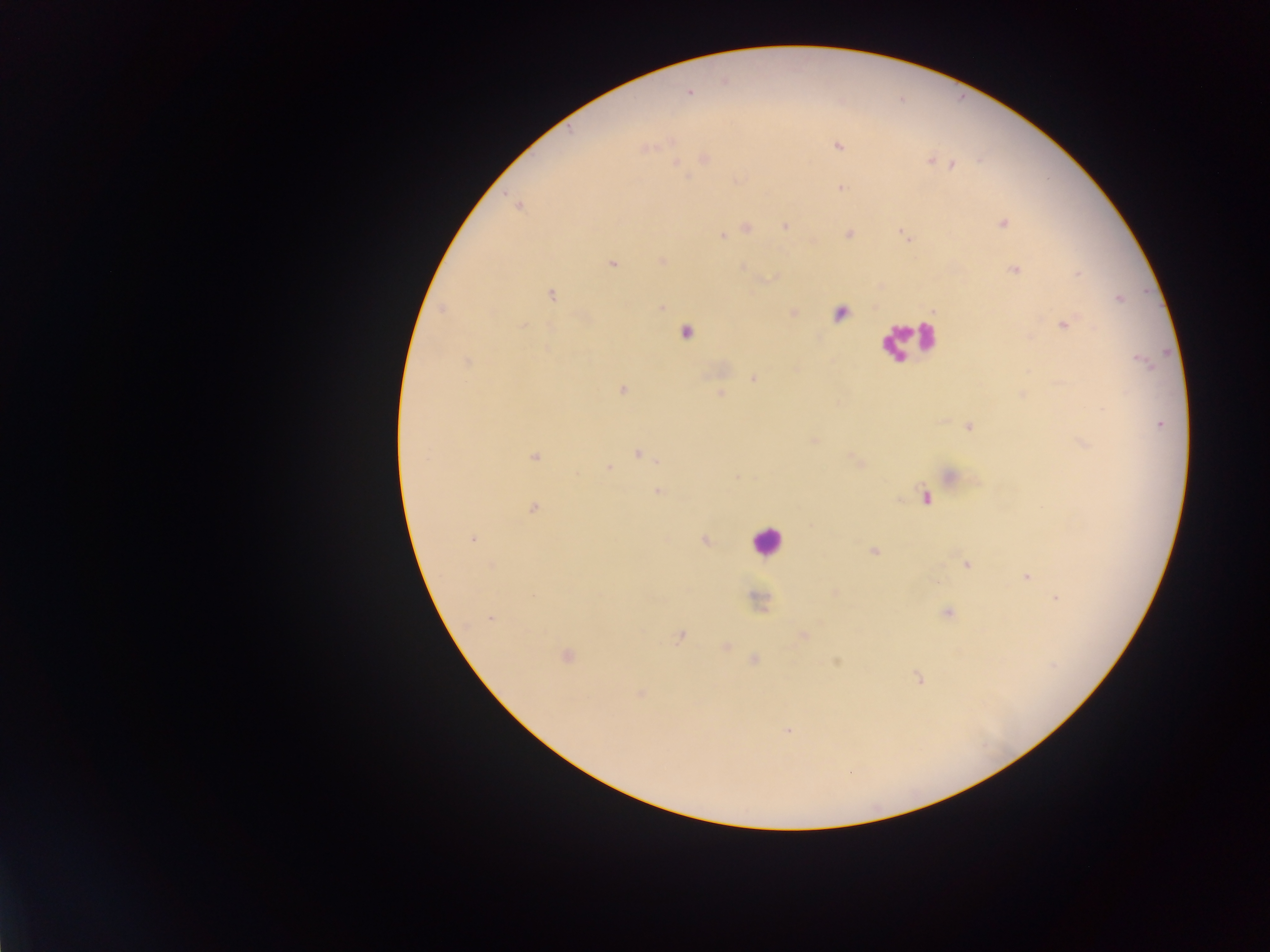 Approximate centers as {x, y} in pixels. Malaria parasite locations: {690, 91}, {837, 145}, {645, 148}, {703, 158}, {929, 160}, {952, 164}, {840, 187}, {1004, 224}, {785, 226}, {747, 227}, {848, 232}, {723, 234}, {661, 260}, {612, 263}, {742, 266}, {1014, 269}, {551, 294}, {1120, 297}, {661, 307}, {440, 309}, {839, 313}, {1064, 323}, {522, 325}, {686, 334}, {1142, 360}, {468, 361}, {753, 376}, {622, 388}, {720, 392}, {1161, 424}, {966, 425}, {814, 439}, {639, 453}, {534, 456}, {656, 460}, {608, 467}, {657, 491}, {926, 496}, {534, 509}, {472, 539}, {704, 540}, {874, 551}, {963, 563}, {491, 565}, {1026, 577}, {1056, 597}, {756, 599}, {946, 612}, {489, 617}, {679, 639}, {834, 663}, {916, 677}, {788, 730}. Leukocyte locations: {767, 545}. Single field of view. Collected in Ghana. Photographed through a microscope with a mobile-phone camera. Image is 1270×952 pixels. Thick blood smear.